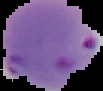
Summary:
  - Image size: 103×91 pixels
  - Malaria status: parasitized
  - Image type: cell region segmented out of the field of view; surrounding area masked to black
  - Preparation: thin blood film